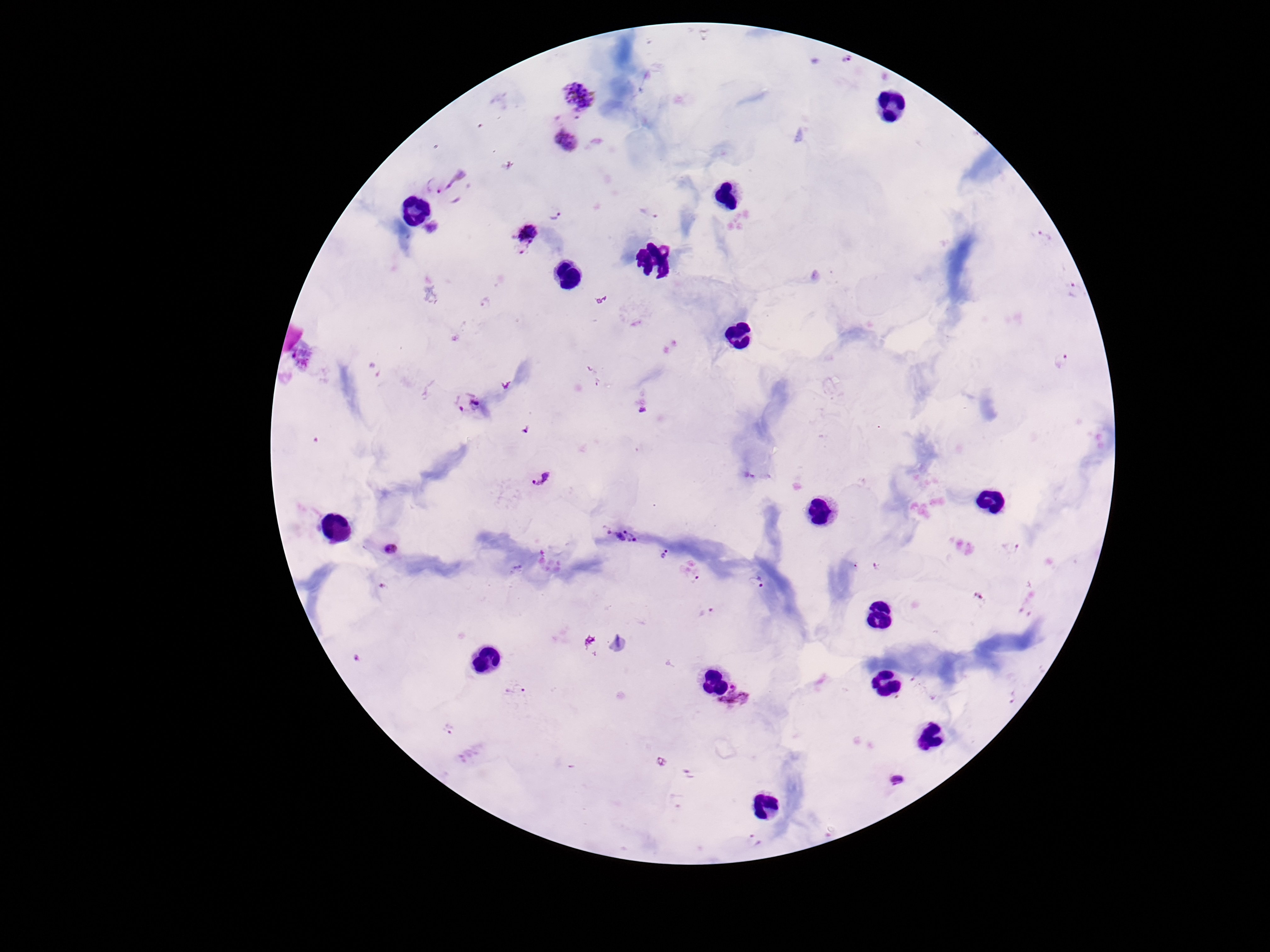
preparation = thick blood smear
image size = 1270×952 pixels
patient malaria status = infected
Plasmodium parasite locations = approximate centers as (x, y) in pixels: (847, 61), (580, 95), (564, 139), (443, 184), (652, 212), (557, 213), (431, 229), (526, 235), (1045, 237), (1075, 291), (486, 304), (1061, 361), (467, 403), (539, 476), (620, 534), (392, 547), (1010, 548), (665, 553), (756, 581), (698, 582), (708, 612), (515, 690), (737, 701), (450, 728), (899, 780), (753, 840)
field of view = single
capture = smartphone camera through the microscope eyepiece
magnification = 100x
stain = Giemsa